Identify the preparation type.
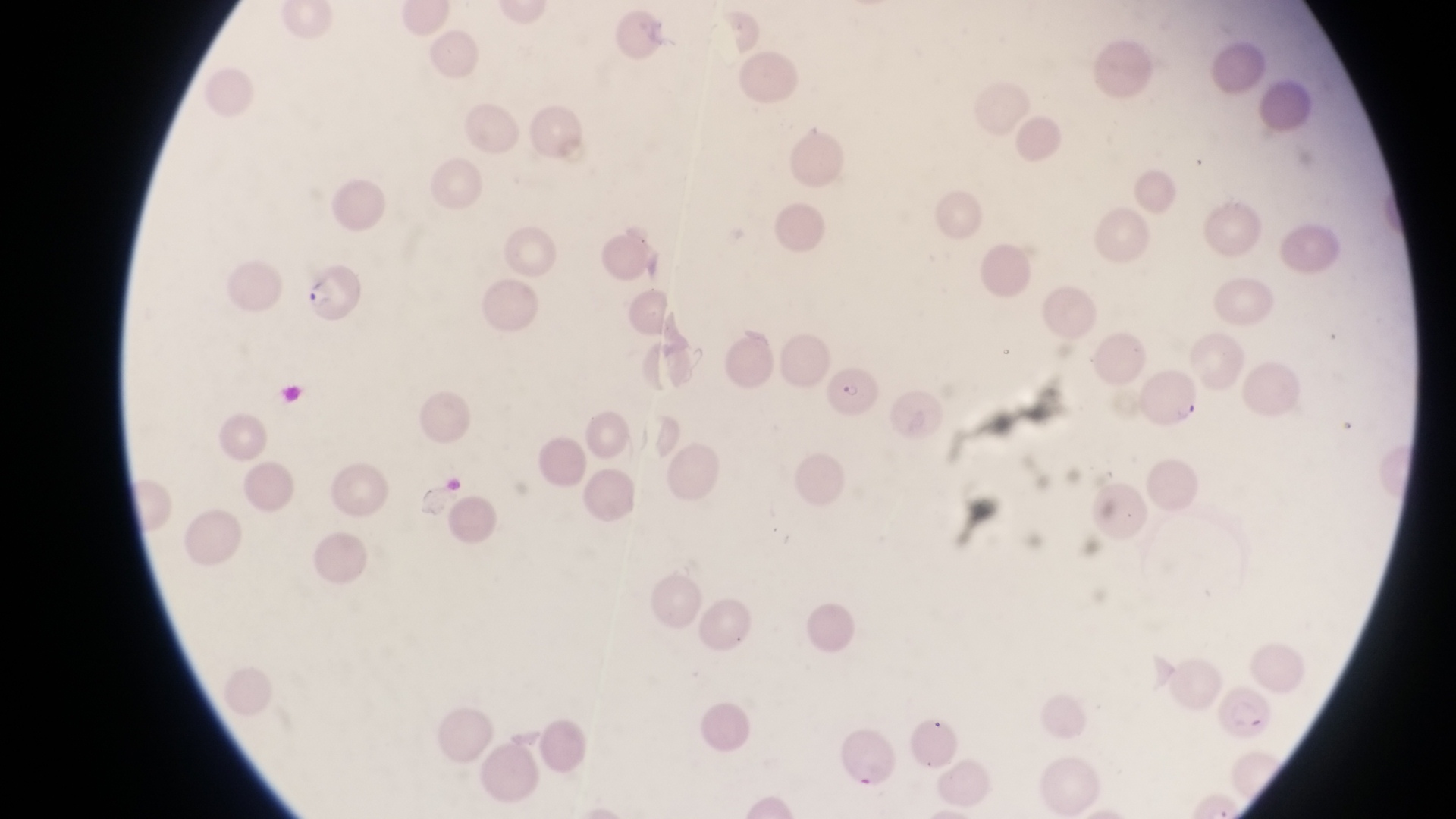

This is a thin smear.

Approximate bounding boxes as (left, top, right, bottom) in pixels. Parasitised red blood cell locations: (290, 274, 362, 319), (829, 364, 887, 420), (1224, 680, 1276, 739). One field of view. Captured by a smartphone held over the eyepiece of an Olympus CX-23 microscope. Image is 1456×819 pixels. At a magnification of 1000x. Collected in Uganda.